Classify this cell by malaria status.
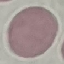

It is uninfected.

Giemsa-stained preparation. Photographed with a smartphone camera at the microscope eyepiece. Thin blood film. Cell patch, automatically extracted from a larger field of view and resized to 64 × 64 pixels.